Comment on the morphology of the red blood cells.
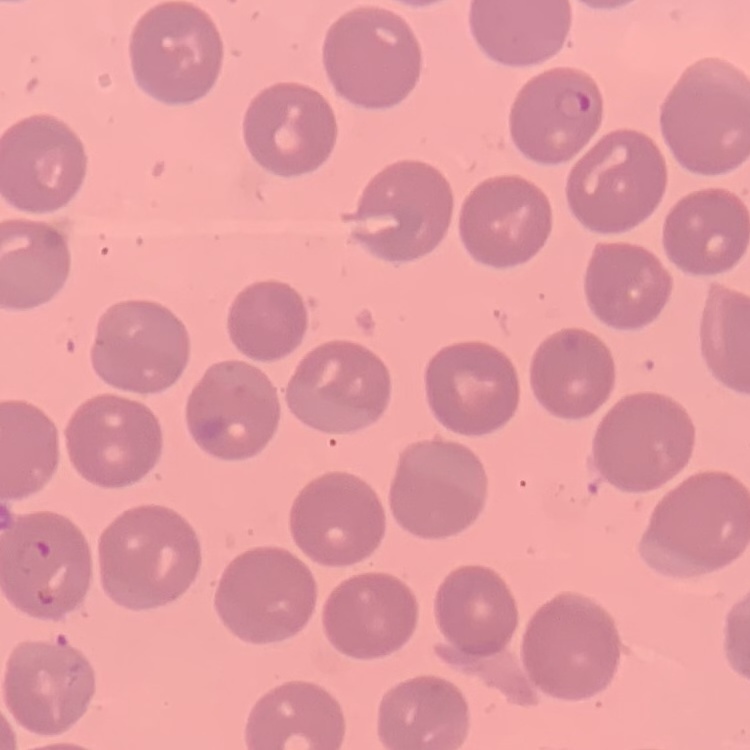

No rouleaux formation.

One tile cut from a larger photomicrograph. Field's or Giemsa stain. Thin blood film.